Assess the morphology of the red blood cells.
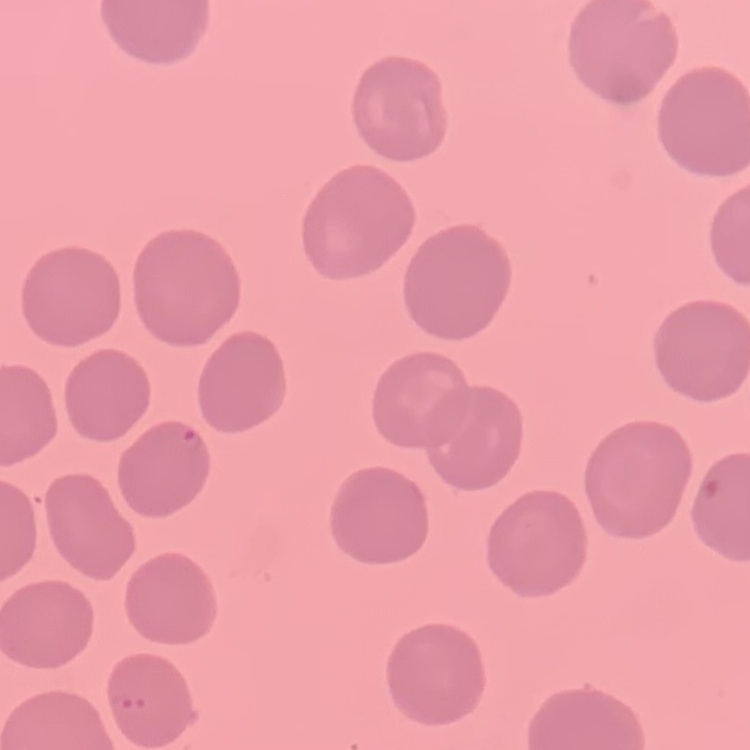

They show no rouleaux formation.

Stained with either Field's or Giemsa. Thin blood film. Square crop of a larger photomicrograph.